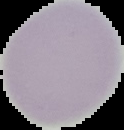
From a thin blood film. Result: no malaria parasites seen. Segmented cell region on a black background. Image is 124×130 pixels.